Assess this cell for malaria.
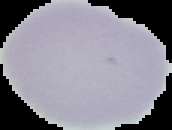
It is uninfected.

Summary:
  - Preparation: thin blood film
  - Image size: 172×130 pixels
  - Image type: cell region segmented out of the field of view; surrounding area masked to black